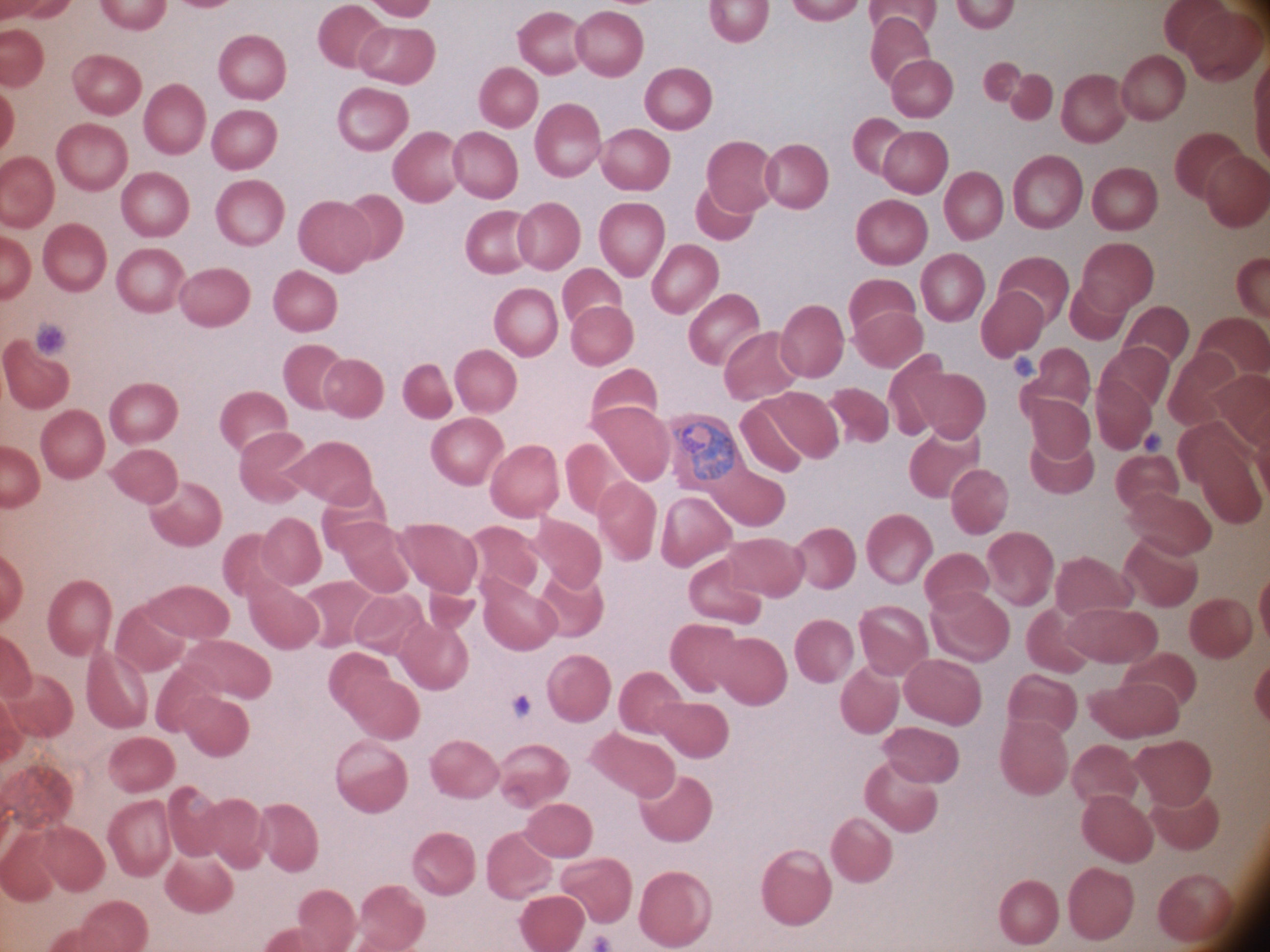

species = Plasmodium ovale
stain = Giemsa
magnification = 100x
microscope = Leica DM2000 with built-in camera
field of view = one from this slide
image size = 1270×952 pixels
trophozoite locations = approximate bounding boxes as named x1/y1/x2/y2 corners in pixels, from the source annotation, which is not necessarily exhaustive: (x1=673, y1=422, x2=734, y2=480)
preparation = thin blood film